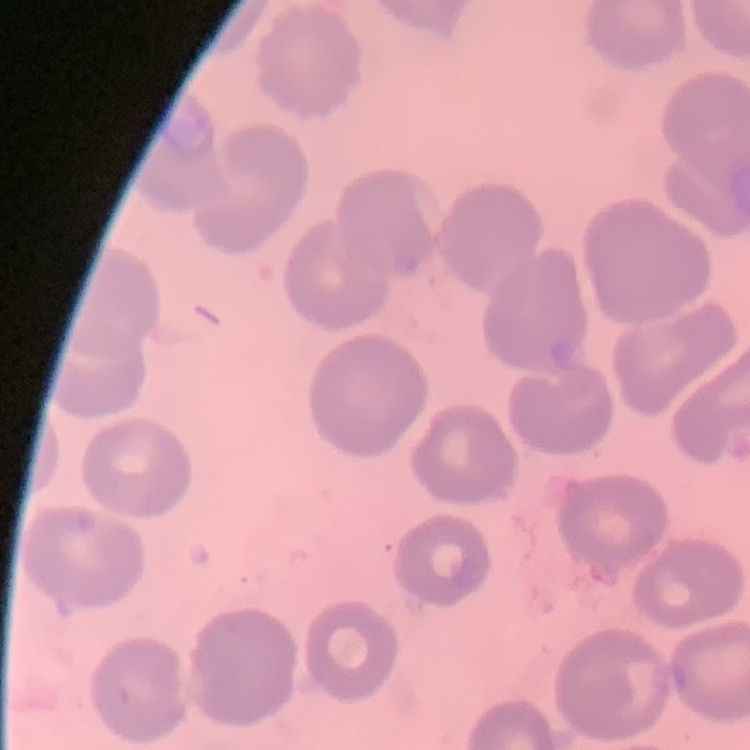
The erythrocytes exhibit no rouleaux formation. Thin blood smear. One tile cut from a larger photomicrograph. Stained with either Field's or Giemsa.